Comment on the morphology of the red blood cells.
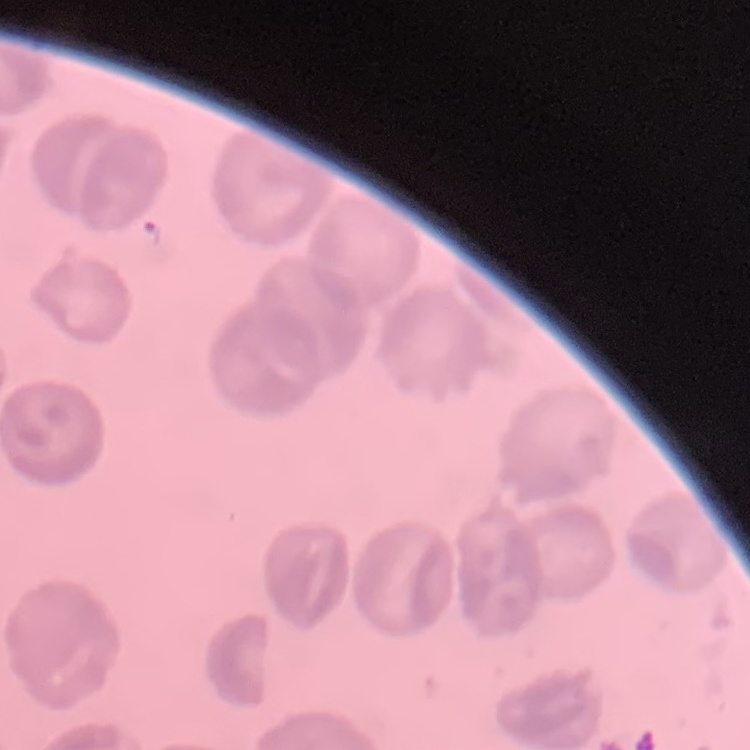

No rouleaux formation.

stain: Field's or Giemsa
preparation: thin blood smear
image_type: one tile cut from a larger photomicrograph